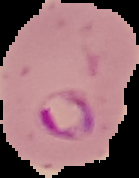

preparation = thin blood smear
image type = segmented cell region on a black background
malaria status = parasitized
image size = 139×178 pixels